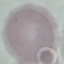

Summary:
  - Malaria status: uninfected
  - Image type: automatically extracted cell patch, resized to 64 × 64 pixels
  - Preparation: thin blood smear
  - Stain: Giemsa
  - Capture: smartphone through the microscope eyepiece